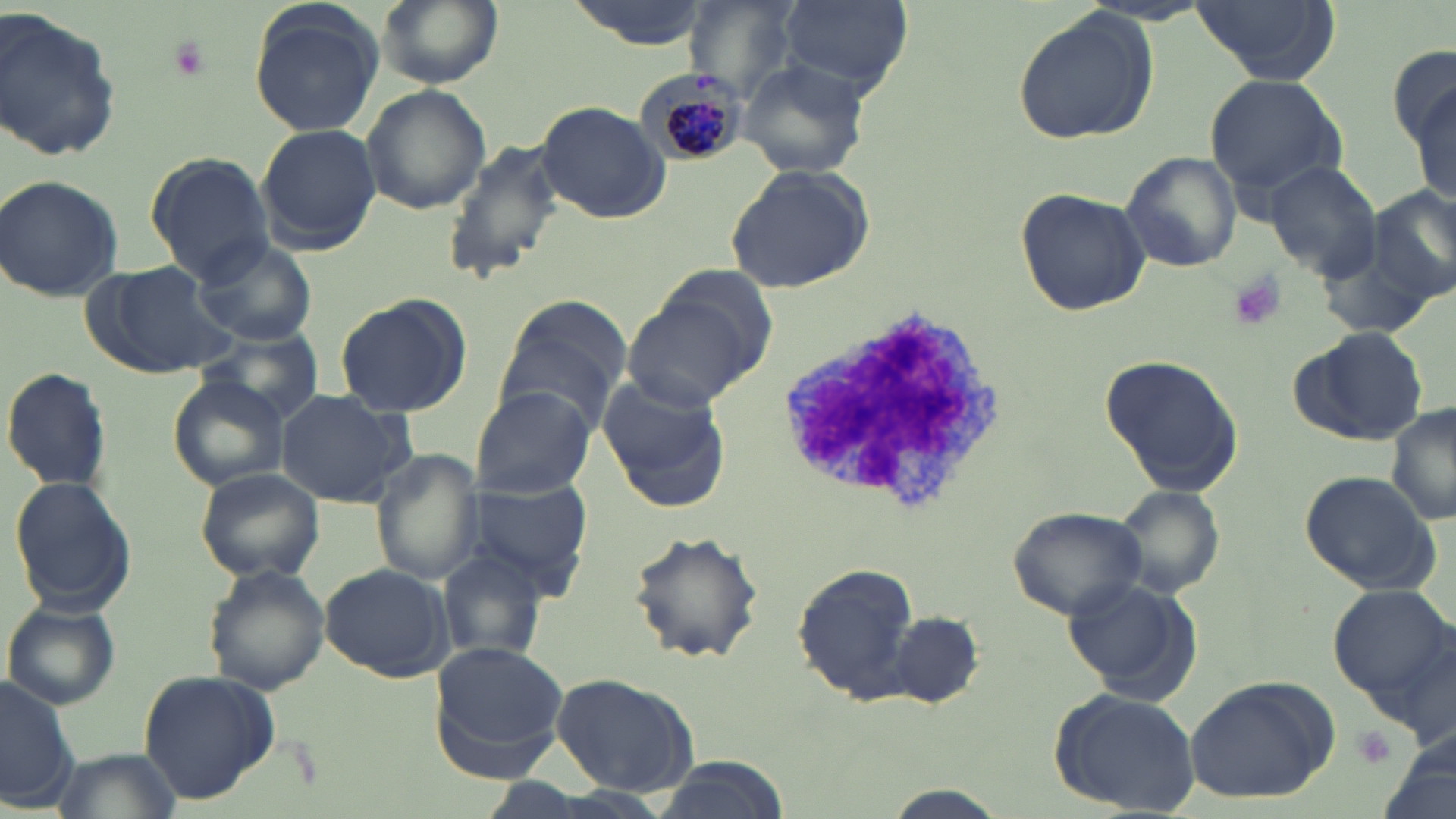

slide-level diagnosis = Plasmodium malariae
field of view = one of a larger specimen
magnification = 1000x
image size = 1456×819 pixels
platelet locations = approximate bounding boxes as named x1/y1/x2/y2 corners in pixels: (x1=163, y1=37, x2=212, y2=81), (x1=1226, y1=272, x2=1288, y2=330), (x1=1349, y1=725, x2=1395, y2=768)
uninfected red blood cell locations = approximate bounding boxes as named x1/y1/x2/y2 corners in pixels: (x1=375, y1=0, x2=505, y2=87), (x1=568, y1=0, x2=707, y2=48), (x1=683, y1=0, x2=797, y2=98), (x1=779, y1=0, x2=911, y2=95), (x1=1191, y1=0, x2=1340, y2=84), (x1=247, y1=1, x2=385, y2=139), (x1=0, y1=7, x2=124, y2=165), (x1=1009, y1=7, x2=1157, y2=147), (x1=1390, y1=43, x2=1456, y2=151), (x1=738, y1=59, x2=870, y2=179), (x1=1203, y1=74, x2=1349, y2=197), (x1=361, y1=86, x2=490, y2=215), (x1=1410, y1=86, x2=1455, y2=204), (x1=535, y1=102, x2=669, y2=222), (x1=256, y1=123, x2=380, y2=254), (x1=439, y1=137, x2=567, y2=287), (x1=1119, y1=151, x2=1243, y2=273), (x1=144, y1=152, x2=274, y2=280), (x1=1263, y1=160, x2=1381, y2=280), (x1=725, y1=165, x2=877, y2=295), (x1=1, y1=173, x2=126, y2=302), (x1=1367, y1=183, x2=1456, y2=308), (x1=1014, y1=187, x2=1148, y2=315), (x1=193, y1=237, x2=318, y2=345), (x1=1317, y1=244, x2=1439, y2=341), (x1=88, y1=259, x2=234, y2=378), (x1=621, y1=275, x2=772, y2=408), (x1=333, y1=295, x2=472, y2=417), (x1=492, y1=296, x2=630, y2=433), (x1=193, y1=325, x2=327, y2=425), (x1=1288, y1=326, x2=1431, y2=447), (x1=1098, y1=351, x2=1246, y2=498), (x1=2, y1=367, x2=114, y2=493), (x1=596, y1=371, x2=732, y2=511), (x1=168, y1=373, x2=290, y2=492), (x1=469, y1=386, x2=595, y2=498), (x1=275, y1=389, x2=414, y2=507), (x1=1387, y1=403, x2=1456, y2=526), (x1=371, y1=450, x2=485, y2=585), (x1=194, y1=467, x2=325, y2=582), (x1=1297, y1=469, x2=1442, y2=596), (x1=9, y1=476, x2=138, y2=614), (x1=460, y1=476, x2=593, y2=597), (x1=1107, y1=482, x2=1228, y2=602), (x1=1006, y1=504, x2=1151, y2=620), (x1=626, y1=528, x2=765, y2=664), (x1=434, y1=551, x2=548, y2=663), (x1=791, y1=562, x2=920, y2=703), (x1=319, y1=563, x2=456, y2=680), (x1=204, y1=565, x2=330, y2=695), (x1=1060, y1=576, x2=1205, y2=704), (x1=1326, y1=586, x2=1456, y2=716), (x1=3, y1=601, x2=120, y2=708), (x1=890, y1=610, x2=986, y2=707), (x1=430, y1=639, x2=574, y2=762), (x1=138, y1=669, x2=278, y2=803), (x1=549, y1=671, x2=700, y2=799), (x1=0, y1=673, x2=83, y2=813), (x1=1183, y1=677, x2=1338, y2=806), (x1=1047, y1=688, x2=1200, y2=816), (x1=54, y1=747, x2=180, y2=818), (x1=650, y1=755, x2=788, y2=819), (x1=872, y1=788, x2=1016, y2=819)
preparation = thin blood smear
stain = May-Grünwald-Giemsa
modality = optical microscopy
white blood cell locations = approximate bounding boxes as named x1/y1/x2/y2 corners in pixels: (x1=773, y1=299, x2=1011, y2=517)
Plasmodium malariae-infected red blood cell locations = approximate bounding boxes as named x1/y1/x2/y2 corners in pixels: (x1=644, y1=73, x2=750, y2=169)